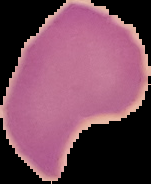

preparation = thin blood film
image type = segmented cell region with the area outside set to black
malaria status = uninfected
image size = 151×184 pixels